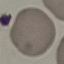 Result: no malaria parasites seen. Thin blood film. Giemsa stain. Acquired by smartphone through the microscope eyepiece. Cell patch, automatically extracted from a larger field of view and resized to 64 × 64 pixels.